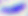
magnification: 400x
identification: Toxoplasma gondii
modality: micrograph